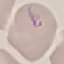

Summary:
  - Result: no malaria parasites seen
  - Image type: automatically extracted cell patch, resized to 64 × 64 pixels
  - Capture: smartphone through the microscope eyepiece
  - Stain: Giemsa
  - Preparation: thin smear